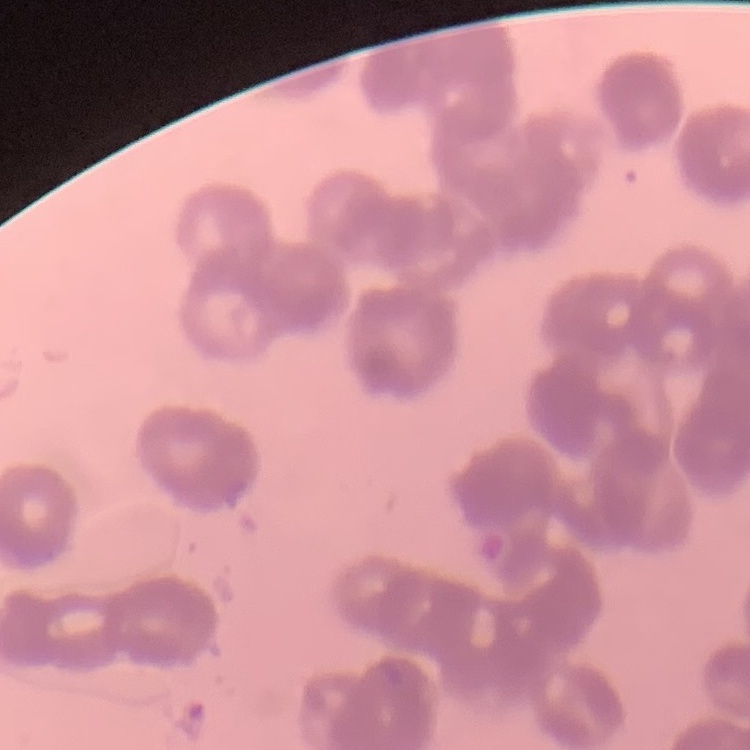
Summary:
  - Erythrocyte morphology: rouleaux formation
  - Stain: Field's or Giemsa
  - Image type: square crop of a larger photomicrograph
  - Preparation: thin blood film